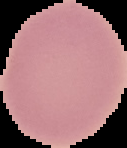
Image is 127×148 pixels. Result: no malaria parasites seen. From a thin blood smear. The area outside the segmented cell region is set to black.